Report the malaria status of this cell.
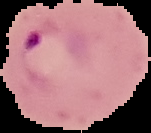
Parasitized.

image type = cell region segmented out of the field of view; surrounding area masked to black
image size = 151×133 pixels
preparation = thin blood smear